Classify this cell by malaria status.
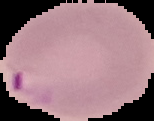
It is parasitized.

Summary:
  - Preparation: thin blood film
  - Image size: 154×121 pixels
  - Image type: cell region segmented out of the field of view; surrounding area masked to black